Classify this cell by malaria status.
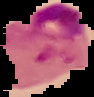
Parasitized.

Summary:
  - Preparation: thin blood smear
  - Image type: segmented cell region with the area outside set to black
  - Image size: 94×97 pixels